Report the malaria status of this cell.
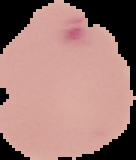

It is parasitized.

Segmented cell region on a black background. Image is 136×160 pixels. From a thin blood film.